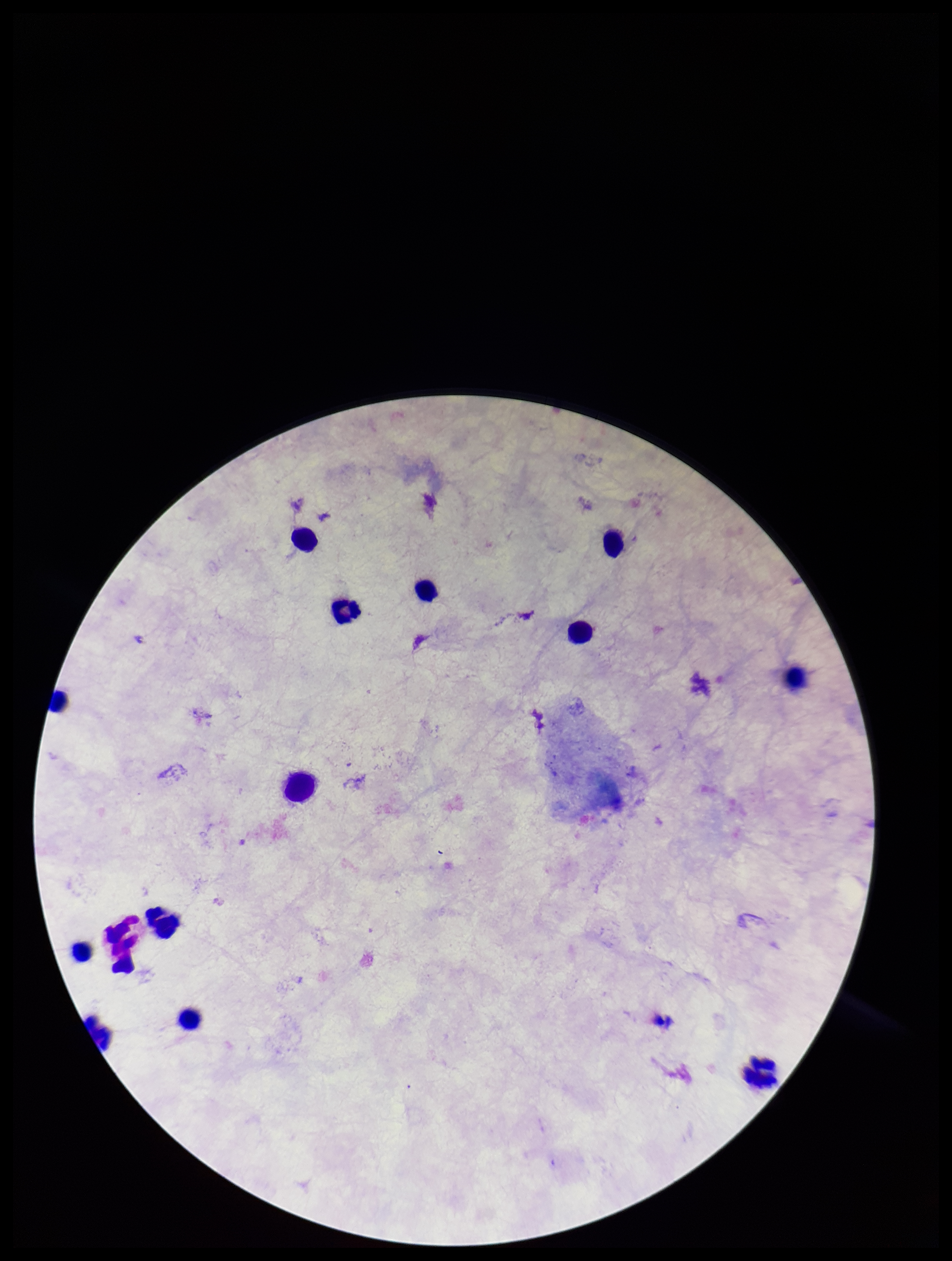

Summary:
  - Capture: smartphone photograph through the microscope eyepiece
  - Preparation: thick smear
  - Leukocyte count: 13
  - Field of view: one from this slide
  - Parasite count: 0
  - Patient malaria status: negative
  - Plasmodium parasites: none seen
  - Stain: Giemsa
  - Image size: 952×1261 pixels